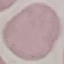 Malaria status: uninfected. Acquired by smartphone through the microscope eyepiece. Cell patch, automatically extracted from a larger field of view and resized to 64 × 64 pixels. Thin smear of blood. Giemsa stain.